Assess this cell for malaria.
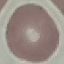
Uninfected.

capture = smartphone through the microscope eyepiece
preparation = thin blood film
stain = Giemsa
image type = cell patch, automatically extracted from a larger field of view and resized to 64 × 64 pixels